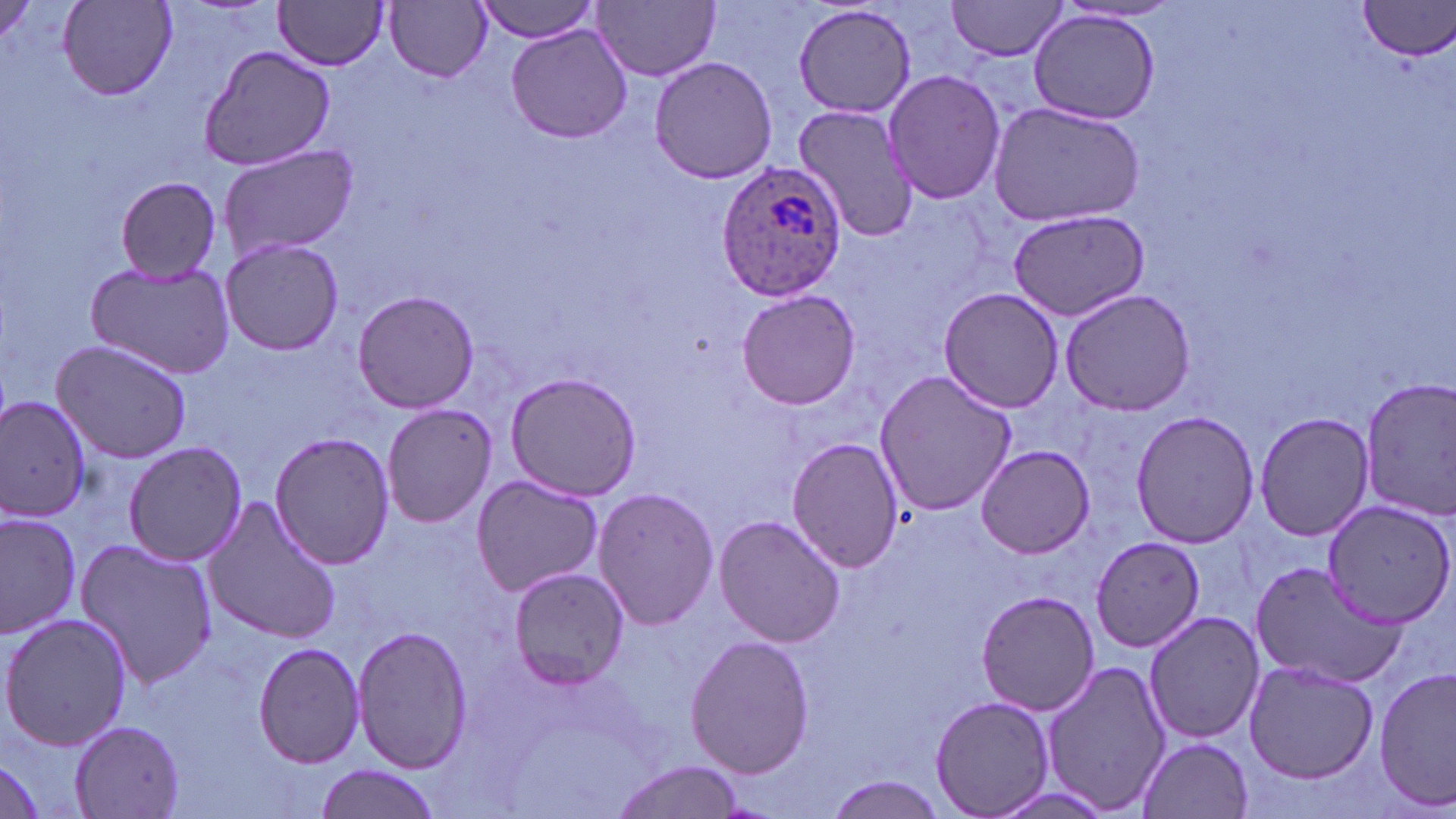

Approximate bounding boxes as (x1,y1)-(x2,y2) corner pairs in pixels. Uninfected red blood cell locations: (472,0)-(604,41), (594,0)-(720,81), (946,0)-(1072,62), (61,1)-(176,98), (272,1)-(392,70), (386,1)-(492,82), (1357,1)-(1456,60), (793,4)-(917,119), (1029,10)-(1161,125), (506,25)-(631,144), (197,43)-(337,173), (649,57)-(776,183), (881,68)-(1006,205), (987,101)-(1146,226), (793,102)-(920,242), (216,144)-(359,264), (114,177)-(223,283), (1005,209)-(1150,320), (218,237)-(345,355), (85,259)-(234,380), (937,286)-(1067,412), (1058,286)-(1196,417), (737,288)-(860,411), (351,289)-(480,414), (50,338)-(193,462), (504,370)-(641,502), (872,370)-(1018,516), (1357,378)-(1456,520), (0,396)-(93,522), (383,404)-(502,526), (1129,410)-(1260,547), (1251,411)-(1376,540), (269,431)-(398,568), (788,437)-(905,571), (123,441)-(246,567), (975,445)-(1096,558), (470,473)-(604,598), (593,485)-(719,631), (202,493)-(341,645), (1322,498)-(1456,628), (0,510)-(82,639), (714,515)-(845,648), (75,537)-(219,691), (1091,537)-(1205,651), (1248,559)-(1404,687), (506,566)-(630,689), (975,589)-(1100,717), (1143,609)-(1264,744), (1,611)-(132,752), (351,626)-(473,774), (685,634)-(814,780), (253,640)-(367,770), (1041,659)-(1171,817), (1245,661)-(1377,783), (1375,668)-(1456,808), (930,696)-(1055,818), (68,719)-(188,818), (1138,736)-(1254,818), (0,751)-(48,818), (606,760)-(746,819), (312,765)-(442,819), (822,776)-(949,819). Plasmodium ovale-infected red blood cell locations: (717,164)-(846,300). Slide-level diagnosis: Plasmodium ovale. 1000x magnification. Light microscopy. May-Grünwald-Giemsa stain. Thin blood film. Image is 1456×819 pixels. One field of a larger specimen.